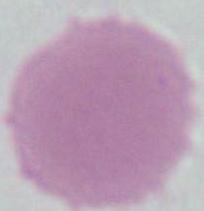 Captured at 1000x magnification. A red blood cell is seen. Photomicrograph.